Give the extent of all Plasmodium ovale-infected red blood cells.
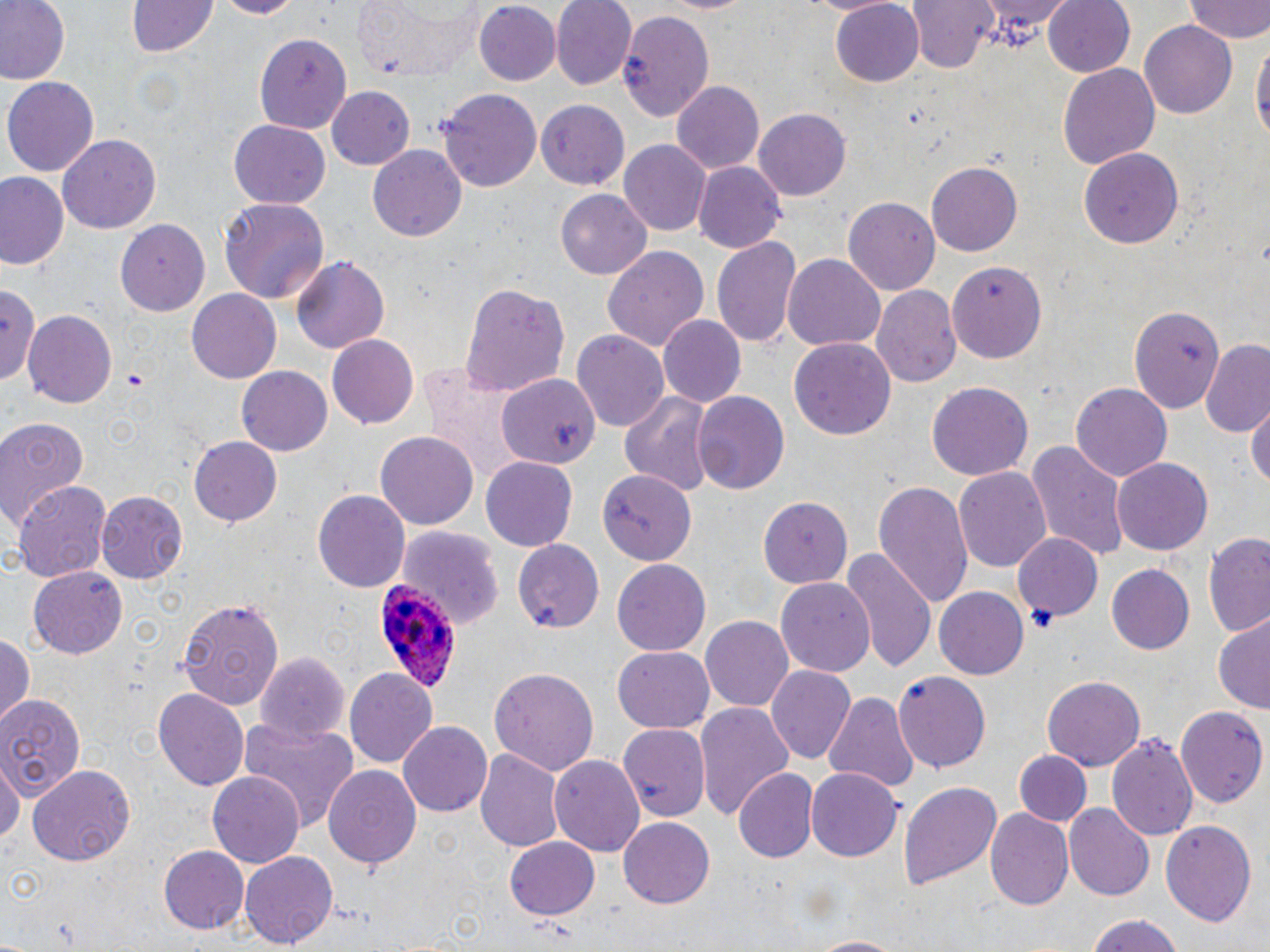
Approximate bounding boxes as (x1,y1)-(x2,y2) corner pairs in pixels.
Plasmodium ovale-infected red blood cells: (376,580)-(466,699).

{
  "slide_level_diagnosis": "Plasmodium ovale",
  "field_of_view": "single",
  "modality": "light microscopy",
  "platelet_locations": "approximate bounding boxes as (x1,y1)-(x2,y2) corner pairs in pixels: (1027,605)-(1056,632)",
  "stain": "May-Grünwald-Giemsa",
  "uninfected_red_blood_cell_locations": "approximate bounding boxes as (x1,y1)-(x2,y2) corner pairs in pixels: (0,0)-(68,84), (127,0)-(219,57), (212,0)-(305,18), (352,0)-(487,81), (550,0)-(638,90), (909,0)-(998,76), (975,0)-(1076,45), (1043,0)-(1135,78), (829,1)-(927,88), (1184,1)-(1270,44), (472,3)-(561,87), (615,9)-(714,120), (1140,20)-(1238,120), (255,34)-(352,133), (1251,34)-(1268,151), (1057,63)-(1159,170), (3,76)-(100,176), (670,81)-(765,174), (327,86)-(416,170), (439,89)-(541,194), (535,100)-(630,188), (753,108)-(849,201), (229,120)-(329,208), (58,134)-(161,235), (617,140)-(712,236), (368,145)-(467,243), (1080,148)-(1186,249), (927,160)-(1023,256), (693,162)-(786,252), (0,172)-(69,271), (555,189)-(652,280), (842,195)-(939,296), (220,199)-(330,303), (115,218)-(209,316), (712,234)-(803,352), (603,245)-(710,351), (782,252)-(885,349), (289,256)-(389,355), (947,259)-(1047,362), (458,281)-(570,396), (871,284)-(961,389), (0,287)-(44,395), (185,289)-(280,382), (1129,301)-(1228,412), (24,309)-(118,410), (658,316)-(747,408), (573,330)-(672,431), (327,333)-(419,426), (789,336)-(894,440), (1199,343)-(1270,436), (235,363)-(332,458), (497,373)-(598,469), (927,383)-(1033,481), (1070,384)-(1171,482), (616,389)-(714,492), (692,391)-(789,497), (1248,404)-(1270,491), (0,417)-(89,530), (377,429)-(478,530), (189,438)-(281,526), (1025,441)-(1131,562), (481,457)-(577,550), (1112,457)-(1214,556), (954,464)-(1052,575), (596,471)-(698,561), (872,477)-(974,611), (12,481)-(114,584), (313,490)-(410,593), (95,491)-(188,583), (759,495)-(853,588), (397,527)-(501,629), (1014,532)-(1101,619), (1202,534)-(1270,640), (515,540)-(605,632), (842,548)-(937,673), (613,560)-(711,656), (1105,563)-(1196,656), (28,566)-(128,657), (776,577)-(878,675), (932,586)-(1029,680), (176,597)-(285,709), (700,616)-(795,712), (1213,616)-(1270,711), (0,635)-(35,725), (614,645)-(712,731), (252,653)-(351,742), (766,665)-(854,763), (344,666)-(438,769), (490,667)-(597,774), (894,670)-(992,773), (1042,674)-(1146,773), (153,688)-(248,793), (822,691)-(916,793), (0,694)-(83,799), (696,701)-(794,820), (1178,705)-(1267,810), (399,720)-(496,817), (238,721)-(357,829), (617,722)-(710,820), (1106,732)-(1197,845), (475,747)-(564,854), (1015,749)-(1091,827), (550,755)-(644,859), (0,757)-(19,854), (29,765)-(136,865), (323,765)-(423,872), (805,767)-(903,863), (734,768)-(819,864), (208,771)-(304,869), (898,779)-(1003,891), (1063,802)-(1154,901), (985,808)-(1073,913), (618,815)-(717,908), (1160,820)-(1258,927), (504,837)-(599,921), (158,846)-(249,935), (242,850)-(338,949), (1082,915)-(1188,952), (801,934)-(908,952)",
  "image_size": "1270×952 pixels",
  "preparation": "thin blood film",
  "magnification": "1000x"
}